Locate every blood parasite and identify its species.
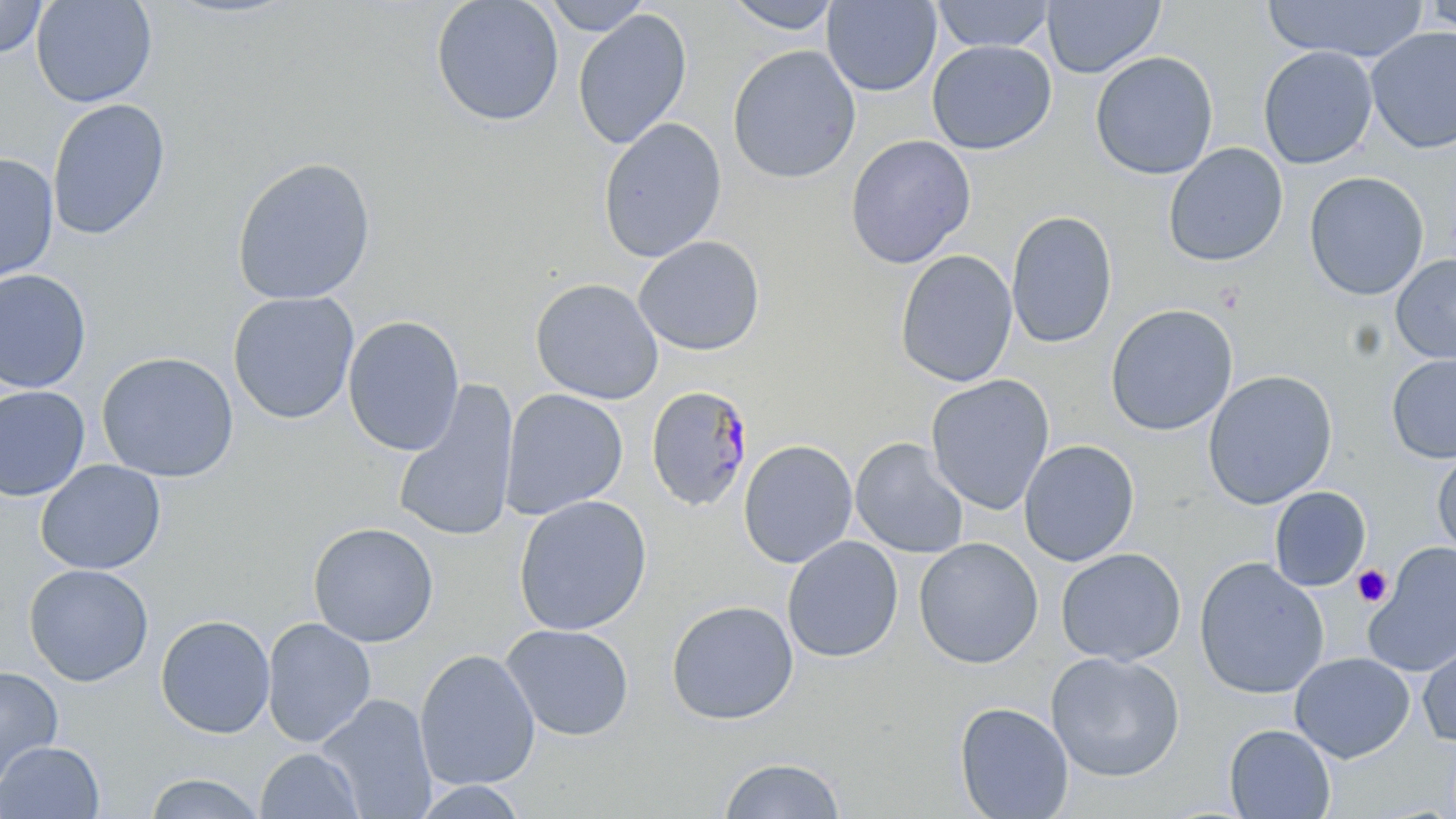

Approximate bounding boxes as [x1, y1, x2, y2] in pixels.
Plasmodium malariae-infected red blood cells: [644, 386, 754, 512].
No Plasmodium falciparum, Plasmodium ovale, Plasmodium vivax, Babesia divergens, or Trypanosoma brucei observed.

Summary:
  - Uninfected red blood cell locations: [0, 0, 48, 58], [31, 0, 157, 108], [430, 0, 565, 128], [541, 0, 653, 36], [721, 0, 843, 34], [1042, 0, 1165, 79], [1264, 0, 1428, 63], [1421, 0, 1456, 38], [821, 1, 942, 97], [931, 1, 1056, 53], [572, 8, 692, 150], [1365, 26, 1456, 154], [926, 40, 1056, 155], [727, 44, 861, 184], [1257, 45, 1378, 170], [1090, 51, 1219, 180], [47, 99, 171, 241], [597, 116, 727, 263], [845, 134, 977, 269], [1162, 143, 1289, 267], [0, 153, 59, 283], [231, 156, 377, 305], [1303, 171, 1429, 301], [1005, 210, 1118, 349], [633, 235, 765, 356], [895, 250, 1018, 387], [1391, 254, 1456, 363], [0, 269, 93, 393], [530, 277, 665, 405], [227, 291, 360, 424], [1104, 304, 1238, 436], [342, 315, 466, 456], [96, 351, 239, 483], [1386, 353, 1456, 464], [1202, 370, 1339, 509], [925, 374, 1055, 515], [392, 380, 520, 544], [0, 386, 90, 501], [500, 388, 628, 521], [850, 437, 969, 559], [738, 439, 858, 569], [1018, 439, 1140, 567], [1431, 449, 1456, 566], [35, 459, 166, 576], [1269, 487, 1371, 591], [512, 494, 652, 636], [307, 522, 439, 647], [782, 536, 904, 663], [913, 537, 1044, 669], [1363, 542, 1456, 676], [1055, 547, 1186, 666], [1193, 557, 1330, 700], [22, 564, 154, 687], [665, 599, 799, 725], [155, 615, 275, 739], [261, 617, 377, 747], [501, 623, 634, 741], [1417, 637, 1456, 747], [414, 648, 540, 791], [1045, 651, 1186, 782], [1289, 652, 1415, 763], [0, 666, 64, 791], [317, 693, 437, 817], [954, 701, 1074, 819], [1223, 724, 1336, 818], [0, 741, 105, 818], [255, 748, 363, 819], [718, 755, 847, 818], [143, 772, 266, 818], [410, 779, 531, 818]
  - Platelet locations: [1352, 565, 1393, 607]
  - Slide-level diagnosis: Plasmodium malariae
  - Image size: 1456×819 pixels
  - Preparation: thin blood film
  - Modality: optical microscopy
  - Field of view: single
  - Magnification: 1000x
  - Stain: May-Grünwald-Giemsa